Classify this cell by malaria status.
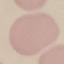
It is uninfected.

Thin blood film. Photographed with a smartphone camera at the microscope eyepiece. Automatically extracted cell patch, resized to 64 × 64 pixels. Giemsa stain.